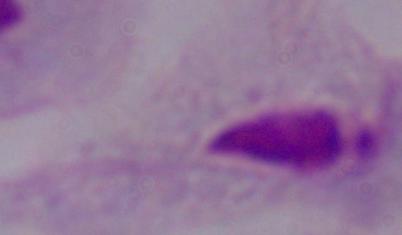
{
  "identification": "trichomonad",
  "modality": "micrograph",
  "magnification": "1000x"
}